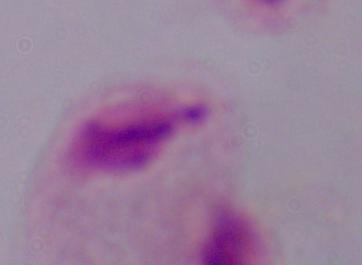

modality = micrograph
identification = trichomonad
magnification = 1000x